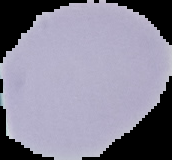
{
  "preparation": "thin blood film",
  "malaria_status": "uninfected",
  "image_size": "172×160 pixels",
  "image_type": "segmented cell region on a black background"
}